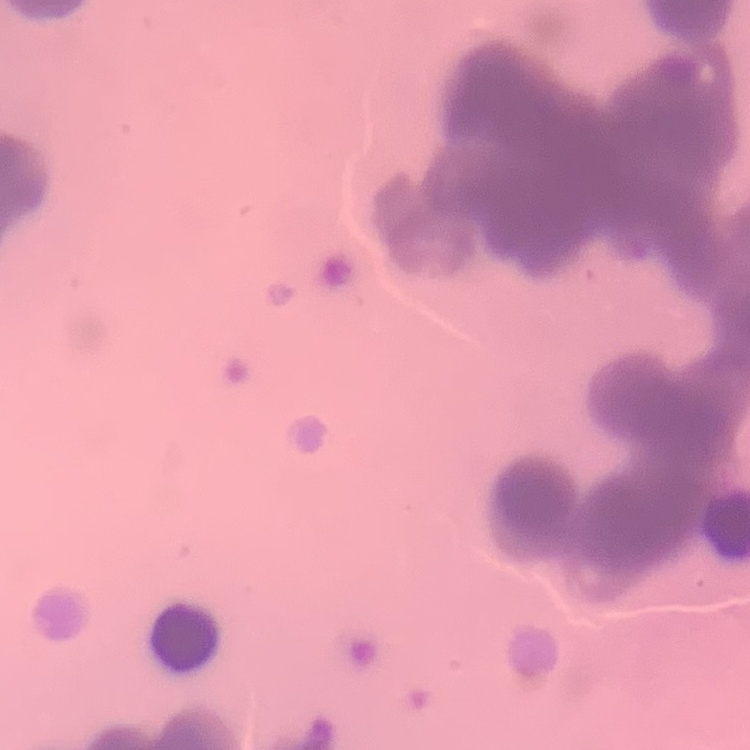

The red blood cells show rouleaux formation. Field's or Giemsa stain. Square crop of a larger photomicrograph. Thin peripheral smear.